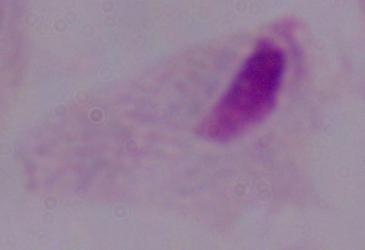

Summary:
  - Magnification: 1000x
  - Identification: trichomonad
  - Modality: micrograph